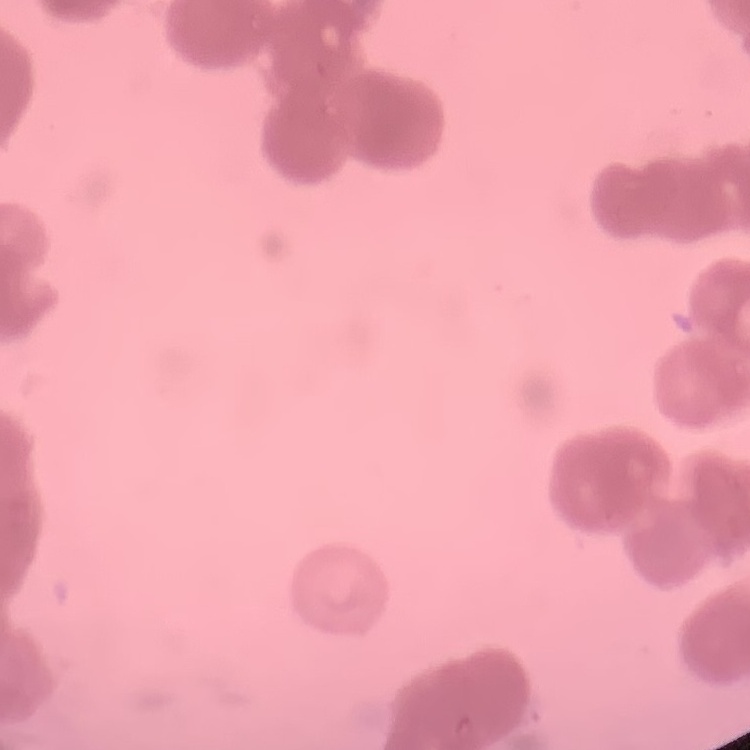

erythrocyte_morphology: rouleaux formation
stain: Field's or Giemsa
preparation: thin blood smear
image_type: square crop of a larger photomicrograph